Outline each blood parasite and name the species.
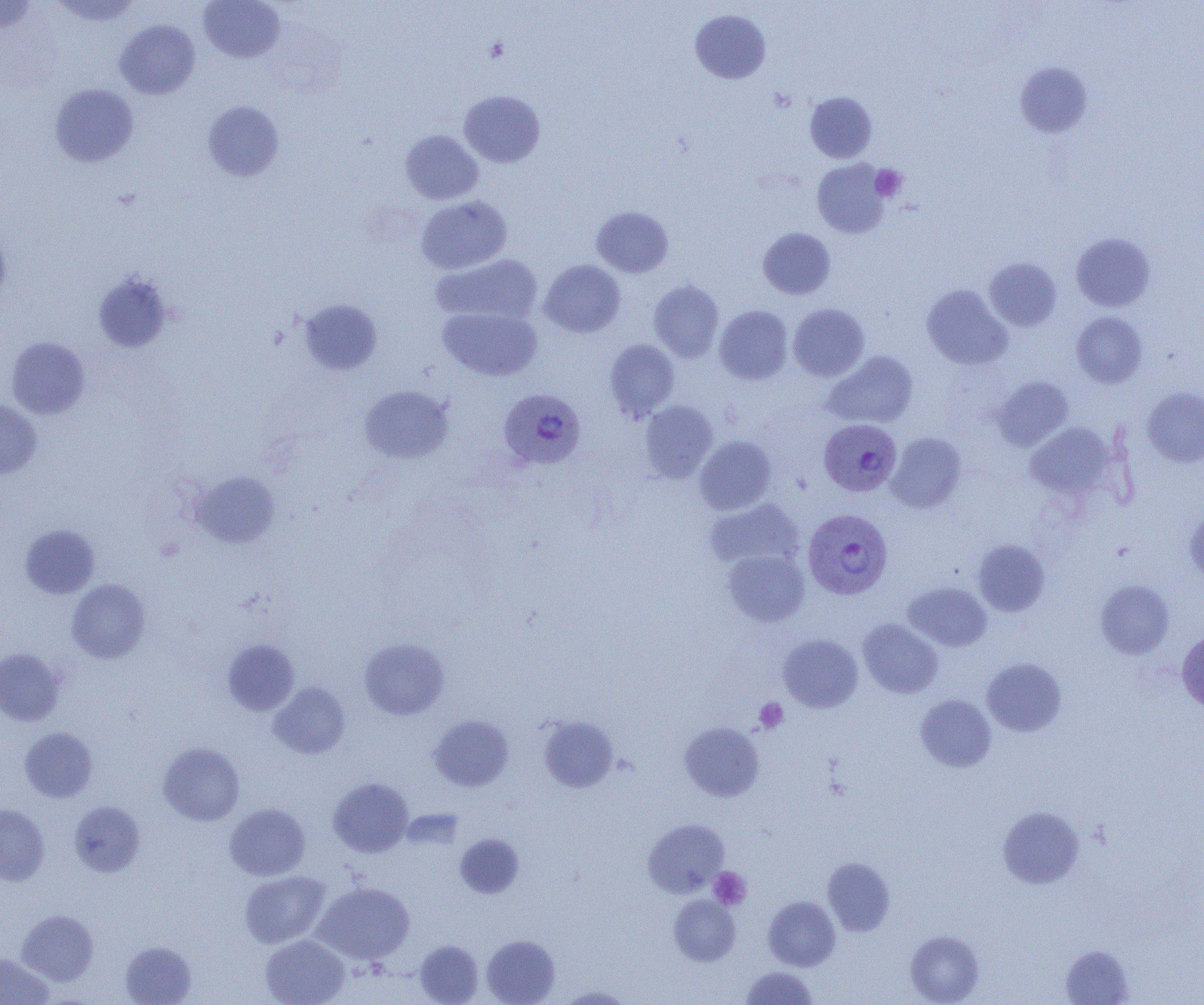
Approximate bounding boxes as (x1, y1, x2, y2) in pixels.
Plasmodium vivax-infected red blood cells: (499, 388, 586, 470), (820, 419, 903, 498), (806, 510, 895, 600).
No Plasmodium falciparum, Plasmodium ovale, Plasmodium malariae, Babesia divergens, or Trypanosoma brucei observed.

Uninfected red blood cell locations: (51, 0, 142, 26), (199, 0, 285, 63), (0, 1, 37, 34), (690, 9, 771, 83), (114, 19, 200, 99), (1015, 62, 1092, 138), (50, 83, 138, 167), (459, 90, 545, 167), (805, 91, 877, 163), (203, 101, 284, 181), (400, 130, 483, 204), (812, 159, 890, 238), (416, 195, 512, 274), (591, 206, 673, 277), (0, 226, 10, 306), (758, 228, 835, 299), (1071, 233, 1155, 311), (432, 253, 543, 326), (984, 257, 1062, 331), (539, 260, 625, 338), (93, 272, 173, 353), (648, 279, 724, 362), (921, 284, 1012, 370), (299, 299, 382, 374), (788, 304, 869, 381), (714, 305, 793, 385), (438, 307, 542, 381), (1071, 311, 1147, 388), (6, 336, 90, 419), (605, 339, 680, 421), (824, 350, 918, 428), (992, 376, 1073, 451), (359, 385, 454, 464), (1142, 387, 1204, 467), (0, 400, 42, 478), (639, 400, 717, 483), (1025, 422, 1116, 500), (886, 433, 966, 513), (695, 436, 777, 515), (189, 471, 279, 548), (705, 498, 805, 571), (1183, 507, 1204, 584), (20, 524, 100, 598), (972, 540, 1050, 616), (723, 550, 809, 626), (67, 579, 151, 663), (1096, 580, 1174, 658), (903, 582, 991, 651), (858, 619, 943, 698), (1177, 629, 1204, 713), (778, 634, 863, 713), (359, 638, 449, 719), (223, 640, 299, 715), (0, 648, 64, 725), (982, 658, 1066, 737), (269, 682, 350, 759), (916, 694, 996, 772), (429, 715, 513, 791), (538, 716, 618, 793), (679, 722, 764, 801), (20, 727, 97, 803), (158, 742, 244, 826), (328, 777, 413, 857), (70, 801, 145, 876), (0, 804, 49, 885), (225, 804, 310, 880), (998, 806, 1085, 889), (401, 809, 464, 850), (643, 819, 730, 897), (455, 834, 524, 898), (822, 857, 895, 935), (240, 871, 330, 948), (312, 882, 414, 965), (669, 895, 740, 966), (763, 896, 840, 971), (16, 909, 99, 986), (905, 931, 984, 1005), (260, 935, 350, 1005), (481, 935, 560, 1005), (415, 940, 483, 1004), (120, 941, 196, 1005), (1061, 945, 1134, 1004), (0, 953, 53, 1005), (740, 966, 818, 1005), (557, 985, 633, 1004). Platelet locations: (870, 164, 906, 201), (755, 698, 788, 733), (709, 867, 751, 909). Slide-level diagnosis: Plasmodium vivax. Optical microscopy. Image is 1204×1005 pixels. Thin blood smear. Captured at 1000x magnification. Single field of view.